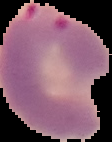
The area outside the segmented cell region is set to black. Image is 112×142 pixels. From a thin blood film. Result: Plasmodium parasites detected.